Classify this cell by malaria status.
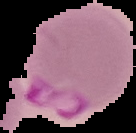

It is parasitized.

image_size: 136×133 pixels
preparation: thin blood film
image_type: segmented cell region on a black background